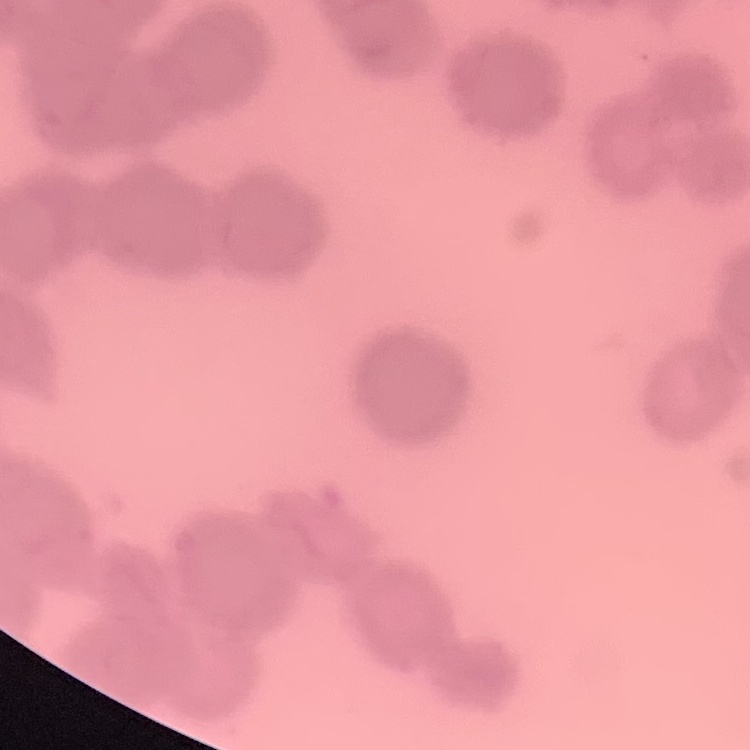

The erythrocytes show rouleaux formation. Field's or Giemsa stain. One tile cut from a larger photomicrograph. Thin blood smear.